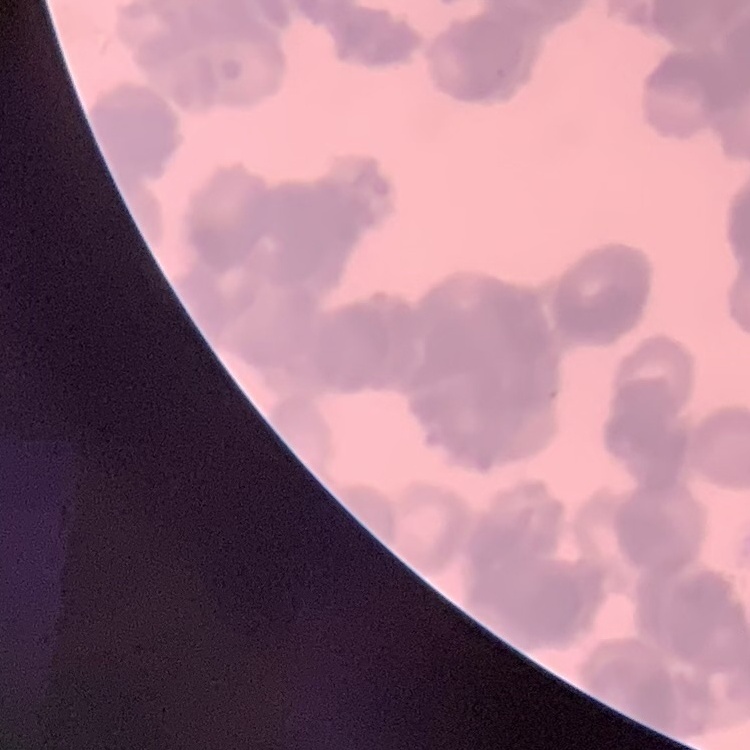
Summary:
  - Erythrocyte morphology: rouleaux formation
  - Image type: square crop of a larger photomicrograph
  - Stain: Field's or Giemsa
  - Preparation: thin peripheral smear